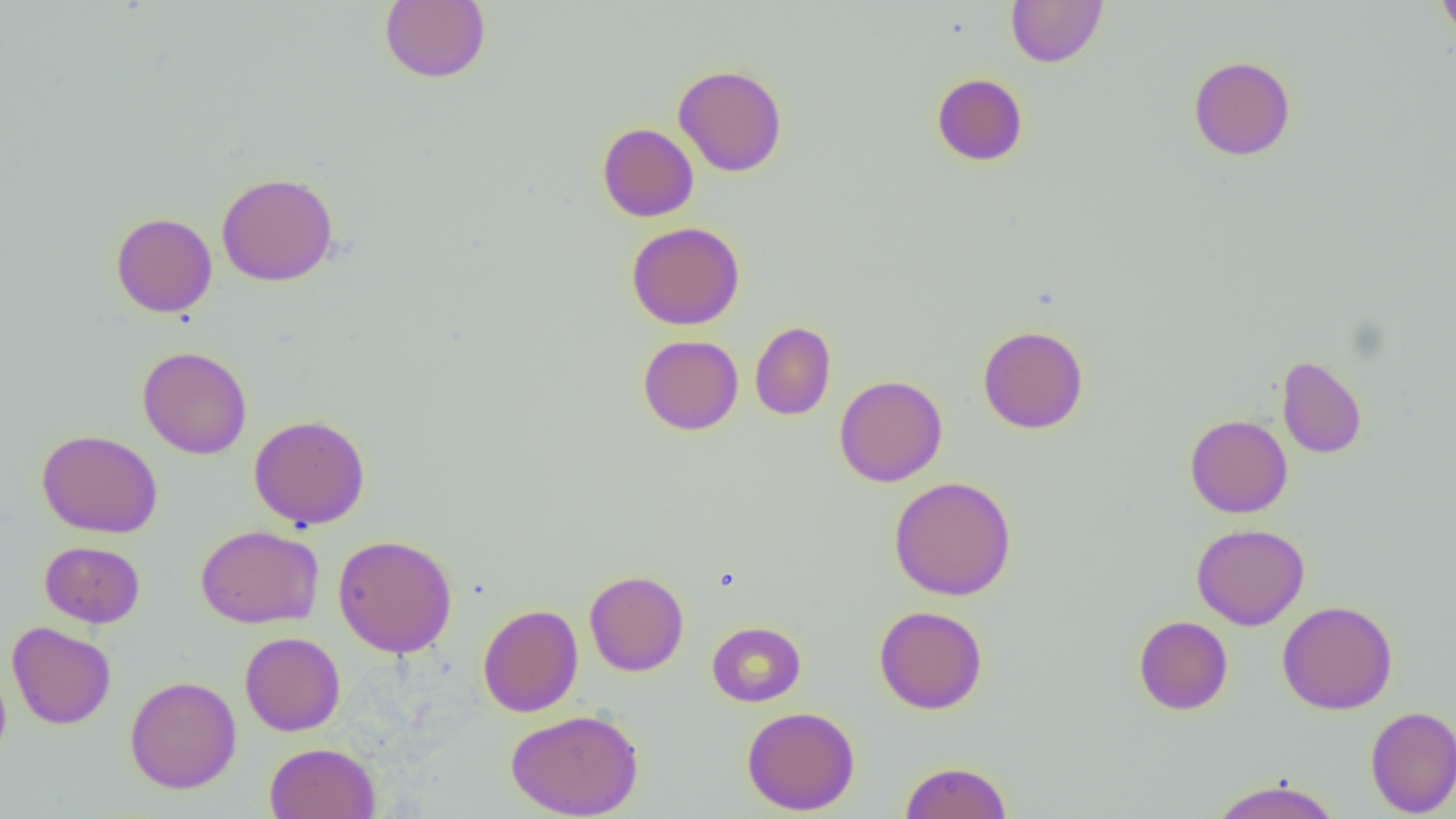
Approximate bounding boxes as [x1, y1, x2, y2] in pixels. Uninfected red blood cell locations: [379, 0, 490, 84], [1006, 0, 1108, 67], [1435, 0, 1456, 42], [1188, 55, 1296, 161], [673, 64, 788, 177], [931, 73, 1028, 166], [597, 123, 699, 222], [216, 172, 338, 286], [110, 212, 217, 317], [626, 222, 745, 330], [750, 321, 836, 420], [977, 325, 1089, 434], [638, 335, 743, 435], [138, 345, 252, 459], [1277, 355, 1367, 458], [834, 374, 948, 487], [249, 414, 370, 530], [1184, 414, 1293, 518], [37, 429, 162, 538], [889, 476, 1017, 600], [195, 524, 323, 628], [1191, 524, 1309, 630], [332, 534, 458, 657], [40, 541, 144, 627], [584, 570, 689, 676], [1277, 600, 1398, 715], [478, 604, 583, 717], [874, 605, 988, 714], [1133, 615, 1233, 715], [707, 621, 806, 707], [7, 622, 117, 729], [240, 632, 345, 736], [0, 660, 11, 769], [125, 675, 241, 794], [741, 706, 860, 815], [1365, 706, 1456, 816], [506, 709, 644, 819], [264, 742, 380, 819], [899, 759, 1013, 819], [1208, 777, 1341, 819]. Slide-level diagnosis: no evidence of blood parasites. One field of a larger specimen. Captured at 1000x magnification. Thin blood film. Image is 1456×819 pixels. Light microscopy.